Name the blood parasite species.
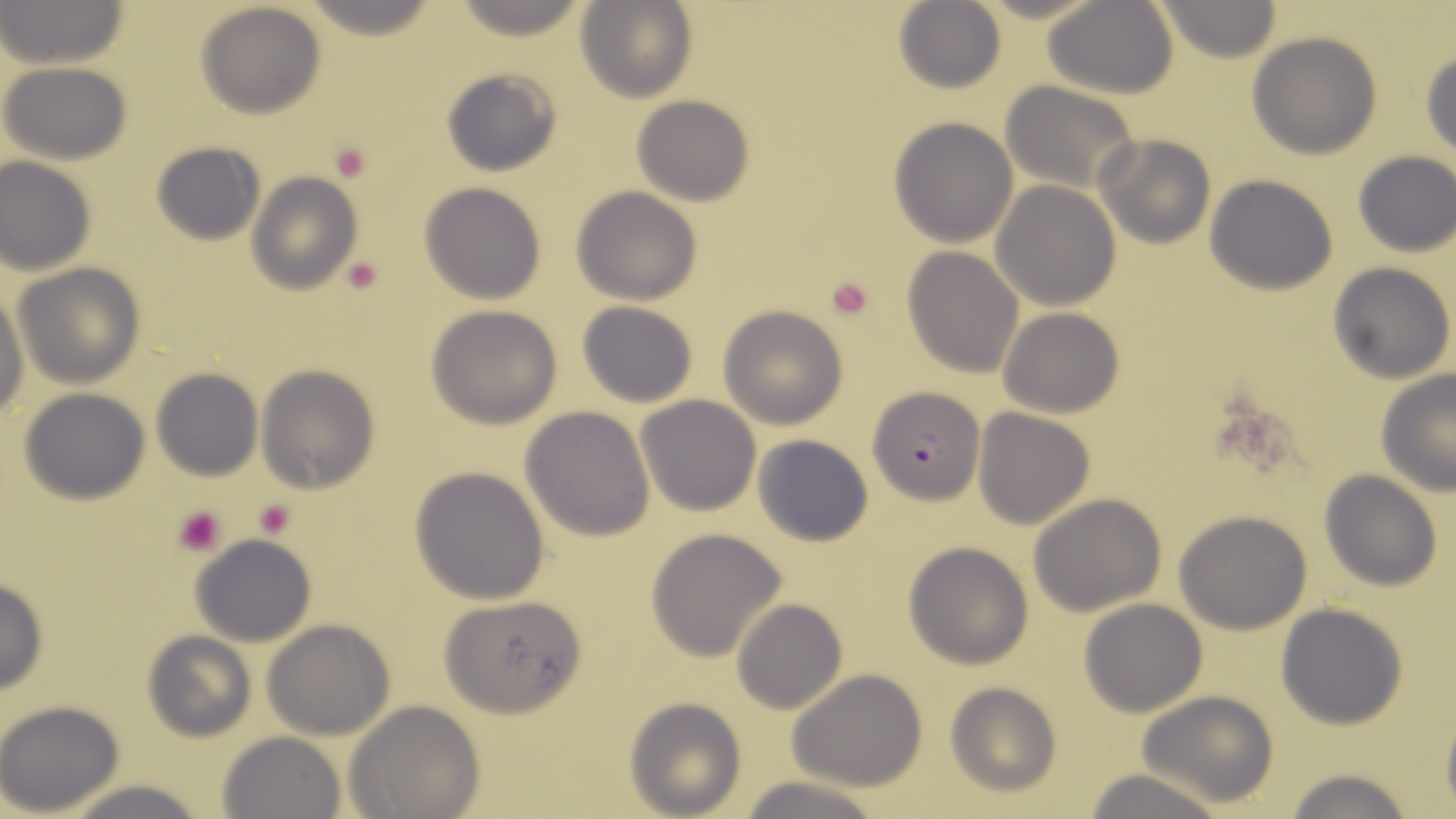
Plasmodium falciparum.

{
  "platelet_locations": "approximate bounding boxes as (x1,y1)-(x2,y2) corner pairs in pixels: (329,139)-(374,180), (342,256)-(383,294), (824,275)-(877,322), (254,496)-(298,539), (171,504)-(228,558)",
  "preparation": "thin blood film",
  "magnification": "1000x",
  "field_of_view": "one of a larger specimen",
  "stain": "May-Grünwald-Giemsa",
  "plasmodium_falciparum_infected_red_blood_cell_locations": "approximate bounding boxes as (x1,y1)-(x2,y2) corner pairs in pixels: (869,385)-(985,505)",
  "uninfected_red_blood_cell_locations": "approximate bounding boxes as (x1,y1)-(x2,y2) corner pairs in pixels: (0,0)-(131,68), (575,0)-(697,104), (1152,0)-(1283,62), (194,1)-(329,120), (1044,1)-(1177,98), (893,2)-(1007,95), (1247,33)-(1382,158), (1421,47)-(1455,159), (2,63)-(133,164), (438,66)-(562,179), (999,82)-(1140,194), (631,93)-(755,205), (887,117)-(1019,248), (1094,133)-(1216,250), (150,144)-(265,247), (1352,152)-(1455,258), (1,156)-(97,275), (246,173)-(361,296), (1204,174)-(1340,295), (418,182)-(547,303), (991,183)-(1120,309), (571,187)-(702,306), (901,247)-(1025,377), (15,263)-(147,389), (1328,263)-(1455,384), (0,288)-(26,417), (578,302)-(698,408), (719,305)-(848,428), (426,306)-(564,427), (997,307)-(1125,418), (256,364)-(381,494), (151,367)-(261,482), (1376,370)-(1456,495), (18,387)-(153,505), (636,395)-(762,516), (520,406)-(655,541), (972,408)-(1095,530), (754,434)-(873,546), (409,465)-(551,604), (1319,470)-(1443,591), (1027,493)-(1167,616), (1173,510)-(1312,634), (646,528)-(788,662), (188,534)-(319,647), (903,541)-(1034,669), (0,578)-(50,694), (437,593)-(590,718), (732,600)-(847,715), (1079,600)-(1207,717), (1275,603)-(1407,728), (262,619)-(395,740), (141,631)-(255,741), (786,670)-(929,790), (944,682)-(1062,799), (1136,690)-(1281,809), (624,698)-(746,817), (0,700)-(126,817), (345,701)-(485,819), (215,731)-(346,819), (1281,765)-(1417,819), (1079,769)-(1230,819), (731,775)-(887,819), (57,779)-(209,818)",
  "modality": "optical microscopy",
  "image_size": "1456×819 pixels"
}